Name the parasite shown.
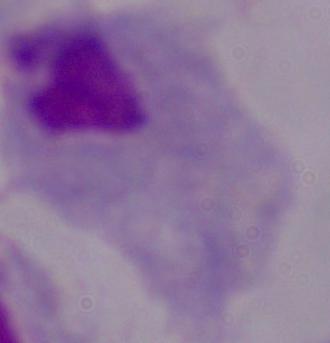
A trichomonad.

Captured at 1000x magnification. Photomicrograph.